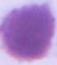

Summary:
  - Modality: photomicrograph
  - Identification: red blood cell
  - Magnification: 1000x